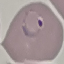

Result: malaria parasites detected. Giemsa-stained preparation. Cell patch, automatically extracted from a larger field of view and resized to 64 × 64 pixels. Thin smear of blood. Photographed with a smartphone camera at the microscope eyepiece.